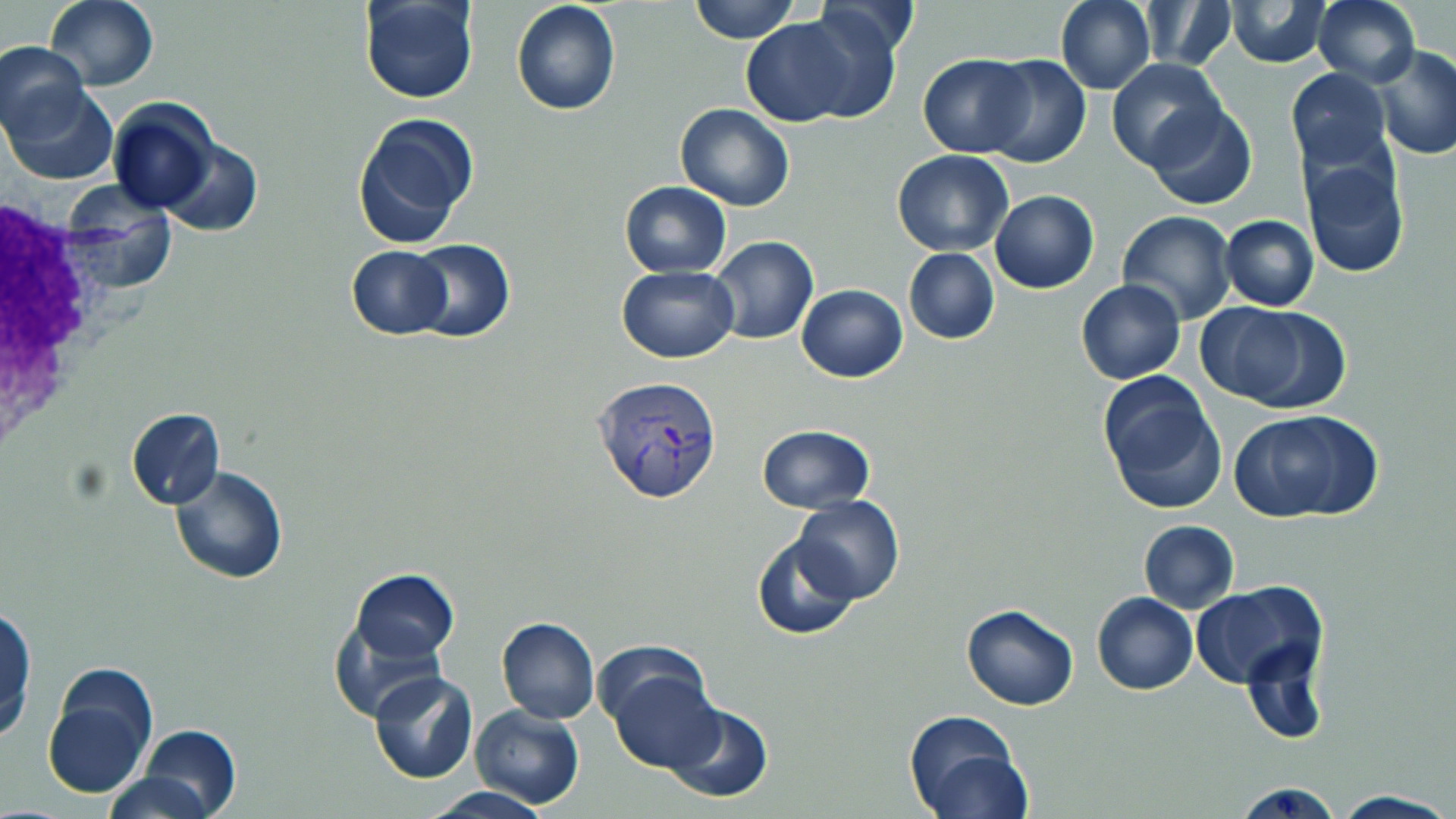
Approximate bounding boxes as (x1, y1, x2, y2) in pixels. White blood cell locations: (0, 193, 115, 462). Plasmodium vivax-infected red blood cell locations: (591, 373, 725, 505). Uninfected red blood cell locations: (45, 0, 158, 90), (690, 0, 796, 43), (1055, 0, 1155, 94), (1226, 0, 1332, 67), (360, 1, 480, 104), (510, 1, 621, 117), (1139, 1, 1236, 71), (1313, 1, 1420, 86), (791, 5, 903, 123), (741, 18, 856, 126), (1, 41, 88, 140), (1370, 45, 1456, 160), (919, 53, 1031, 157), (980, 55, 1091, 168), (1106, 57, 1225, 171), (1284, 69, 1392, 171), (5, 83, 118, 184), (108, 98, 219, 214), (676, 103, 795, 213), (1145, 103, 1257, 210), (352, 112, 479, 249), (159, 139, 262, 236), (892, 148, 1013, 255), (1300, 157, 1411, 278), (619, 181, 731, 276), (989, 190, 1099, 293), (1117, 211, 1237, 326), (1220, 214, 1319, 310), (706, 236, 818, 345), (404, 239, 515, 343), (345, 246, 453, 339), (903, 248, 999, 344), (617, 266, 739, 362), (1076, 279, 1186, 385), (796, 284, 907, 381), (1222, 305, 1354, 413), (1095, 371, 1225, 514), (126, 408, 225, 510), (1229, 408, 1384, 523), (755, 425, 876, 513), (169, 466, 289, 584), (792, 496, 904, 603), (1138, 521, 1239, 612), (751, 536, 858, 640), (350, 569, 457, 661), (1188, 581, 1327, 690), (1092, 592, 1197, 696), (960, 605, 1078, 710), (0, 606, 36, 742), (331, 608, 453, 724), (497, 615, 600, 724), (1239, 633, 1332, 742), (601, 657, 723, 773), (41, 662, 159, 800), (369, 671, 478, 783), (661, 702, 773, 804), (471, 705, 585, 809), (905, 709, 1031, 818), (136, 725, 241, 818), (105, 771, 220, 818), (1232, 780, 1344, 819), (420, 788, 553, 819), (1330, 791, 1456, 819). Slide-level diagnosis: Plasmodium vivax. Light microscopy. Image is 1456×819 pixels. Single field of view. Thin blood smear. May-Grünwald-Giemsa stain. 1000x magnification.